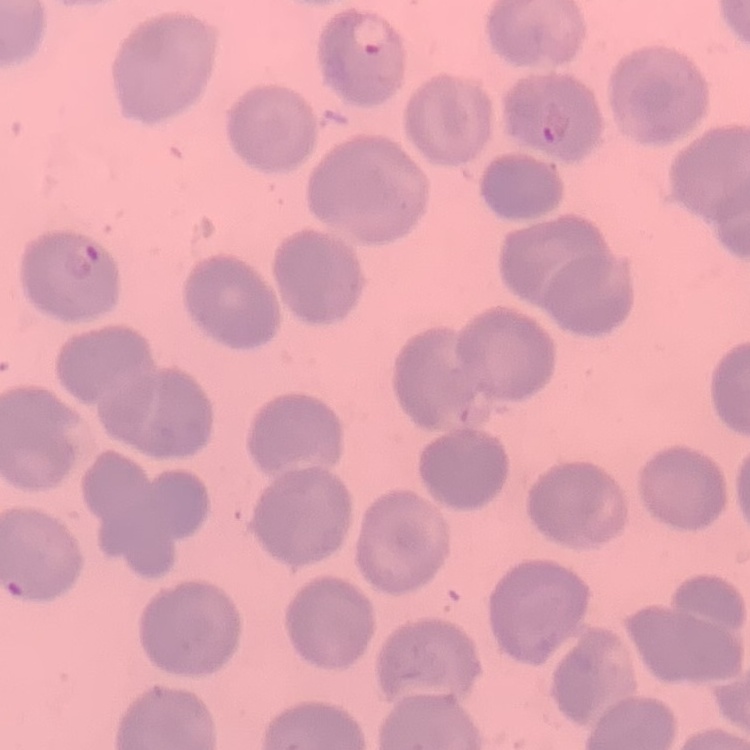
The erythrocytes show no rouleaux formation. Square crop of a larger photomicrograph. Stained with either Field's or Giemsa. Thin blood film.